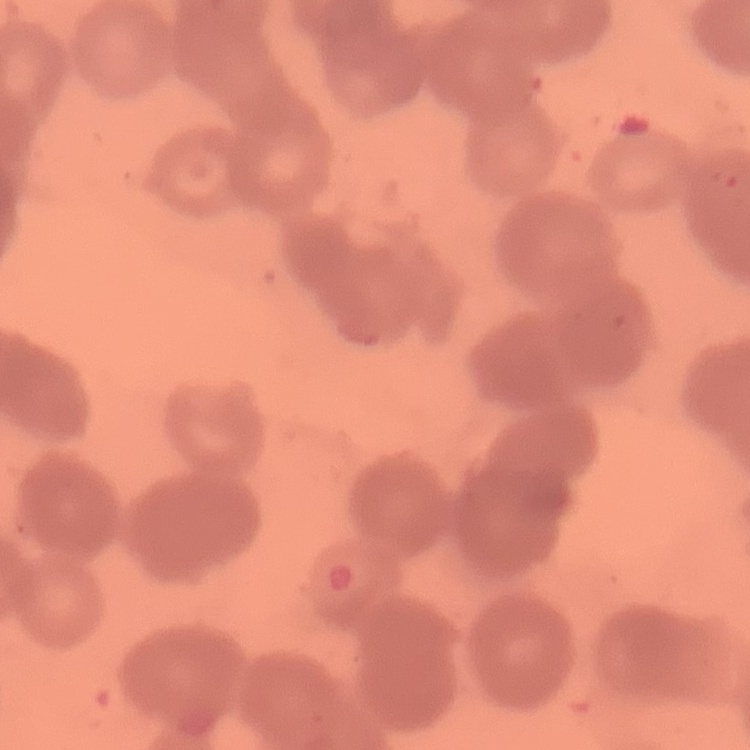 The erythrocytes exhibit rouleaux formation. Thin blood film. Square crop of a larger photomicrograph. Stained with either Field's or Giemsa.